Name the parasite shown.
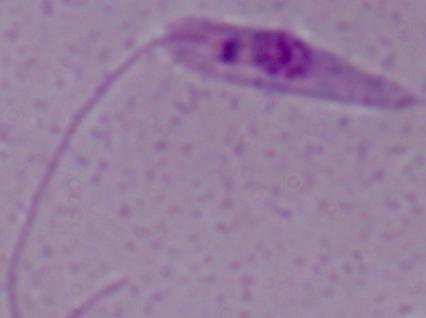
This is Leishmania.

Micrograph. 1000x magnification.